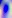 Toxoplasma gondii is seen. Photomicrograph. Captured at 400x magnification.